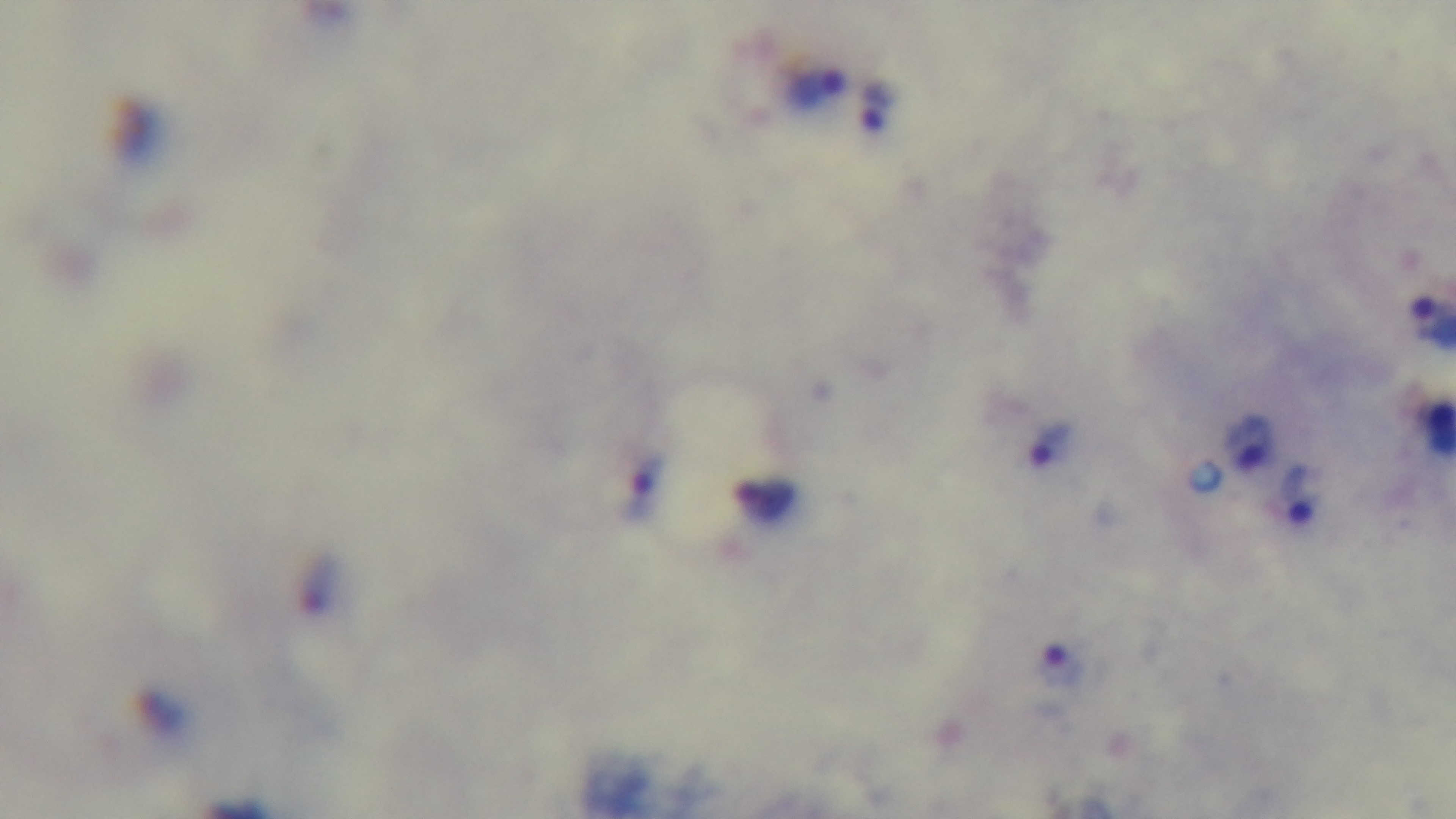

Summary:
  - Stain: Giemsa
  - Objective: 100x oil immersion
  - Preparation: thick blood film
  - Field of view: single
  - Capture: mounted 4K digital camera
  - Malaria status: positive
  - Modality: light microscopy